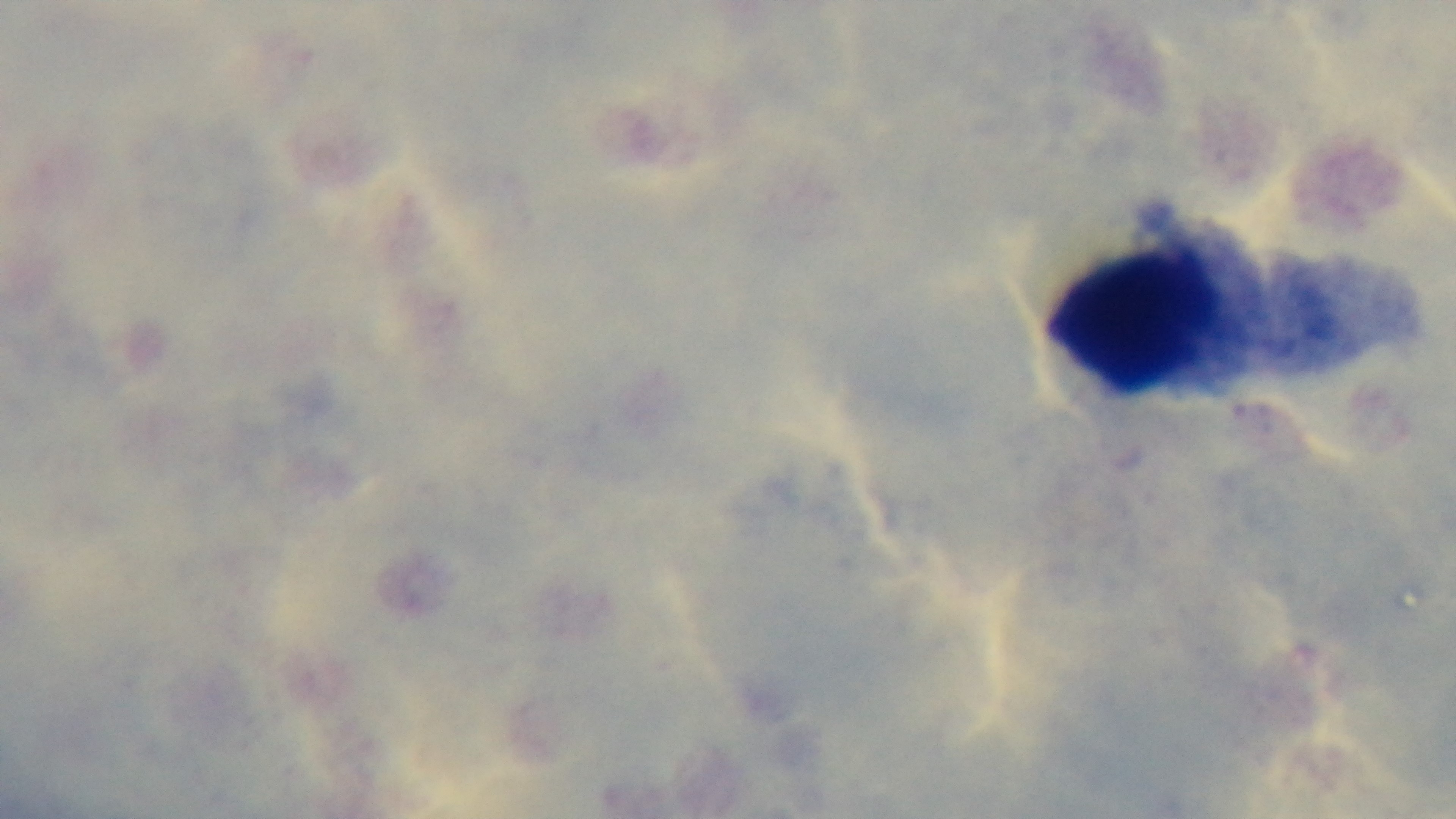

Summary:
  - Preparation: thick blood film
  - Capture: mounted 4K digital camera
  - Modality: light microscopy
  - Malaria status: negative
  - Objective: 100x oil immersion
  - Stain: Giemsa
  - Field of view: one from the slide